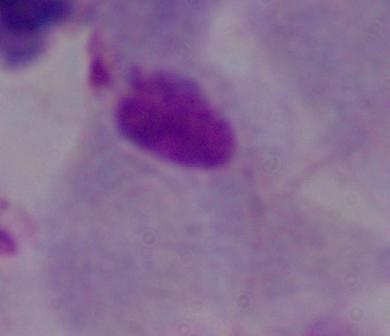

{
  "magnification": "1000x",
  "identification": "trichomonad",
  "modality": "photomicrograph"
}